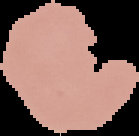

Summary:
  - Result: no malaria parasites seen
  - Image type: segmented cell region with the area outside set to black
  - Image size: 139×136 pixels
  - Preparation: thin blood film